Identify the cell.
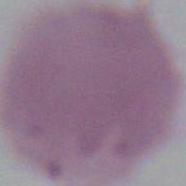
An erythrocyte.

Summary:
  - Modality: micrograph
  - Magnification: 1000x